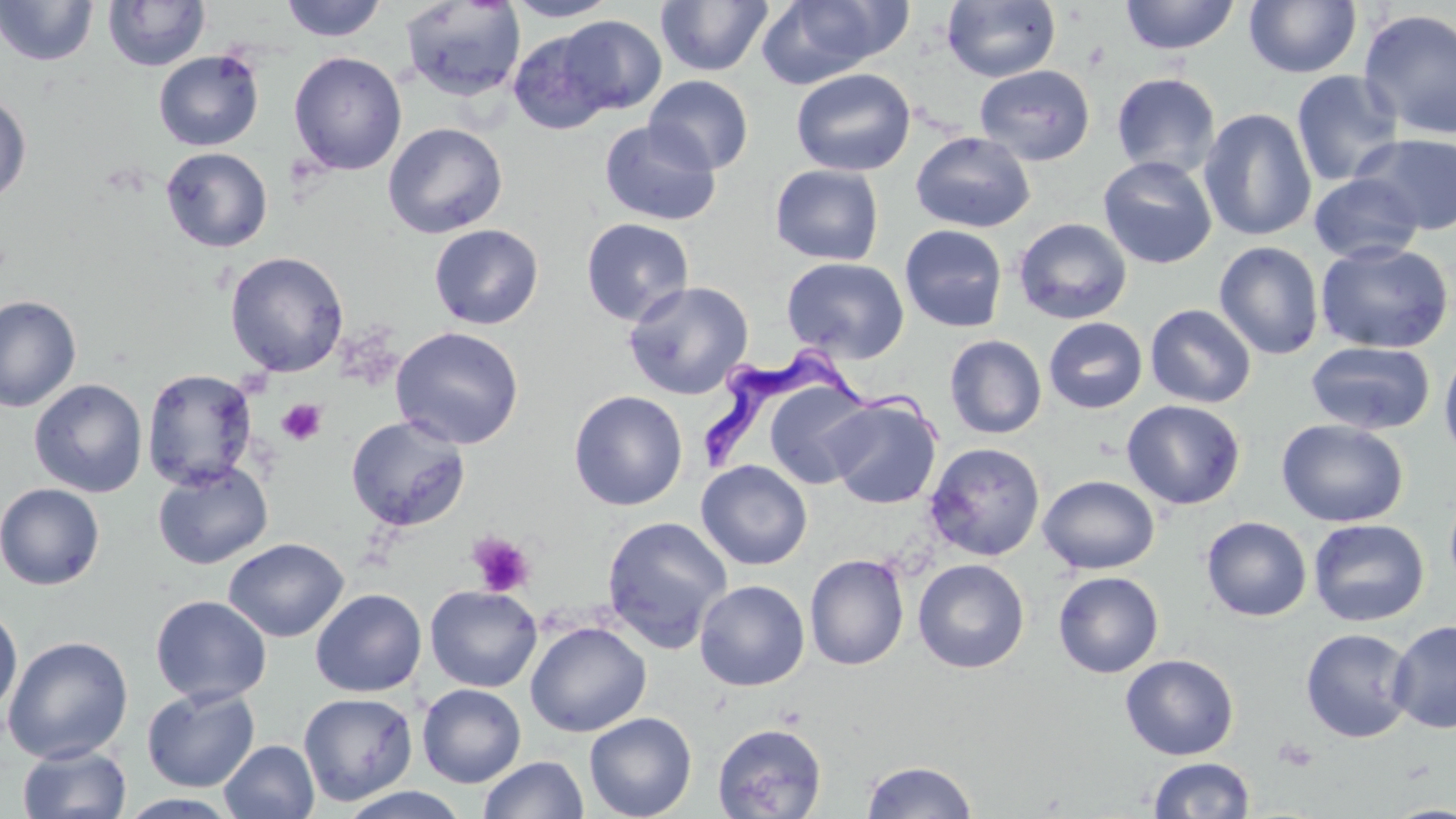

Summary:
  - Coordinate format: approximate bounding boxes as [x1, y1, x2, y2] in pixels
  - Platelet locations: [276, 399, 326, 446], [467, 531, 535, 598], [1274, 737, 1320, 772]
  - Uninfected red blood cell locations: [0, 0, 98, 66], [280, 0, 387, 42], [504, 0, 621, 22], [655, 0, 774, 77], [755, 0, 910, 87], [1120, 0, 1239, 55], [1244, 0, 1362, 78], [102, 1, 211, 71], [399, 1, 526, 102], [942, 1, 1060, 82], [1358, 8, 1456, 141], [555, 15, 667, 115], [508, 30, 614, 135], [153, 50, 265, 151], [288, 51, 407, 176], [974, 65, 1095, 166], [791, 68, 916, 177], [1290, 70, 1405, 187], [1111, 72, 1222, 178], [644, 75, 754, 175], [0, 91, 32, 207], [1198, 107, 1317, 242], [599, 120, 722, 226], [382, 122, 508, 238], [909, 131, 1035, 233], [1352, 132, 1456, 235], [161, 147, 273, 252], [1098, 156, 1218, 269], [769, 164, 884, 266], [1308, 172, 1424, 265], [1013, 217, 1132, 325], [581, 218, 695, 326], [428, 224, 544, 330], [899, 224, 1008, 332], [1214, 241, 1324, 360], [1315, 241, 1454, 354], [225, 251, 349, 377], [781, 256, 910, 363], [622, 280, 755, 399], [0, 295, 82, 413], [1145, 304, 1257, 408], [1043, 317, 1148, 414], [390, 325, 525, 449], [944, 334, 1047, 439], [1305, 340, 1435, 435], [1439, 347, 1456, 465], [142, 368, 258, 491], [29, 378, 147, 497], [763, 379, 876, 489], [568, 389, 688, 511], [824, 395, 942, 509], [1121, 399, 1246, 510], [345, 415, 471, 532], [1276, 418, 1409, 528], [924, 442, 1045, 561], [696, 460, 812, 571], [152, 462, 273, 569], [1037, 475, 1160, 574], [0, 482, 105, 590], [1444, 487, 1456, 595], [601, 515, 732, 652], [1200, 516, 1312, 622], [1308, 519, 1429, 627], [223, 537, 349, 642], [805, 554, 909, 670], [913, 558, 1030, 674], [1053, 571, 1164, 678], [694, 579, 810, 691], [425, 585, 542, 692], [310, 588, 427, 697], [151, 595, 272, 706], [0, 604, 23, 717], [1388, 619, 1456, 734], [525, 620, 652, 737], [1299, 627, 1416, 743], [2, 635, 134, 764], [1120, 654, 1239, 760], [417, 683, 526, 787], [141, 686, 260, 792], [298, 692, 417, 806], [584, 712, 697, 819], [712, 723, 827, 818], [219, 740, 320, 819], [17, 743, 132, 819], [478, 755, 587, 818], [1148, 757, 1255, 818], [862, 760, 977, 818], [333, 785, 474, 818]
  - Trypanosoma brucei locations: [696, 345, 944, 466]
  - Slide-level diagnosis: Trypanosoma brucei
  - Preparation: thin blood film
  - Stain: May-Grünwald-Giemsa
  - Modality: optical microscopy
  - Magnification: 1000x
  - Field of view: one of a larger specimen
  - Image size: 1456×819 pixels